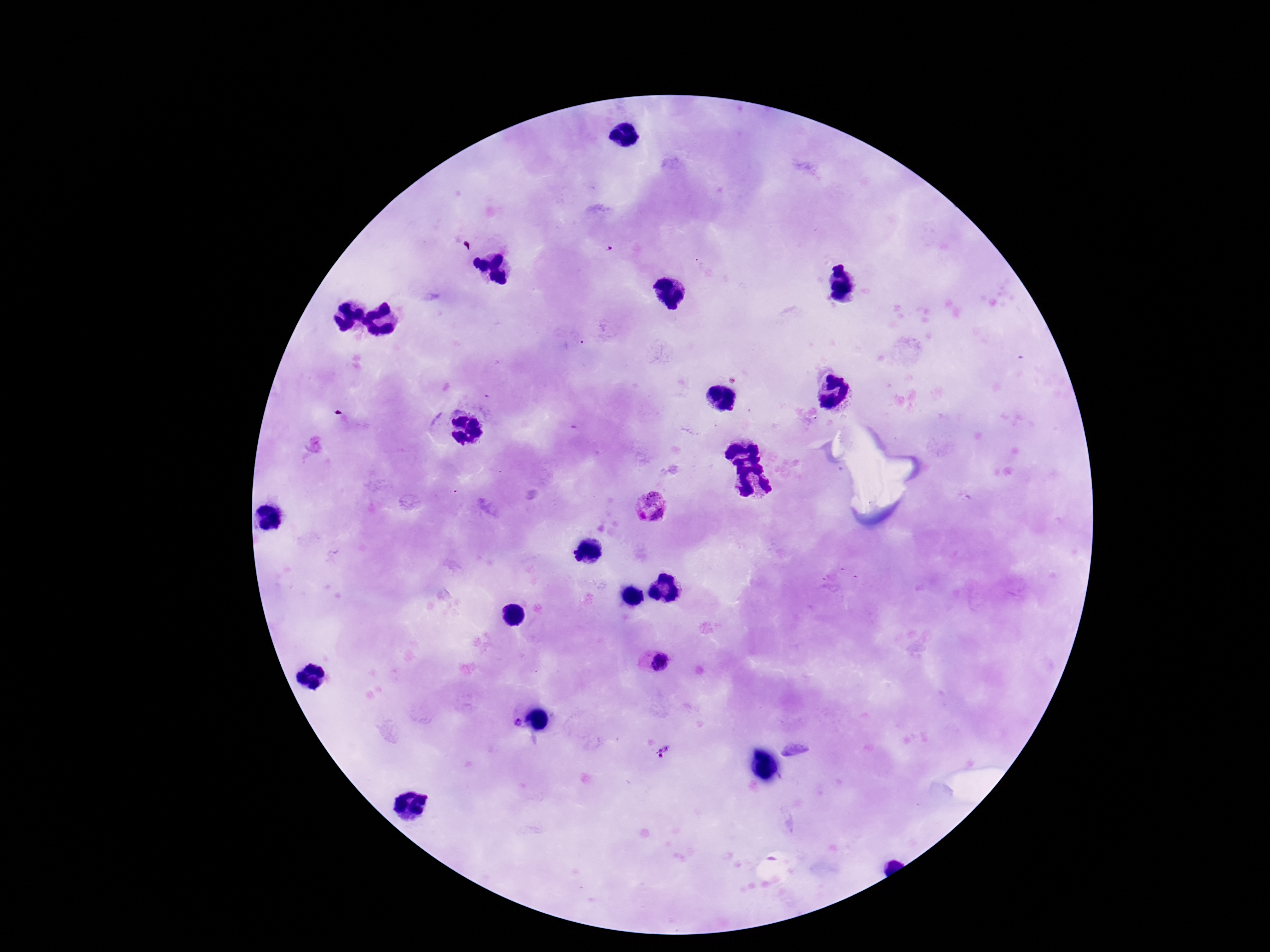

{
  "field_of_view": "single",
  "image_size": "1270×952 pixels",
  "stain": "Giemsa",
  "capture": "smartphone camera through the microscope eyepiece",
  "preparation": "thick blood film",
  "patient_malaria_status": "positive",
  "magnification": "100x",
  "plasmodium_parasite_locations": "approximate centers as (x, y) in pixels: (650, 504), (655, 664), (515, 724), (663, 751)"
}